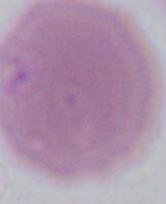
Summary:
  - Modality: photomicrograph
  - Magnification: 1000x
  - Identification: red blood cell